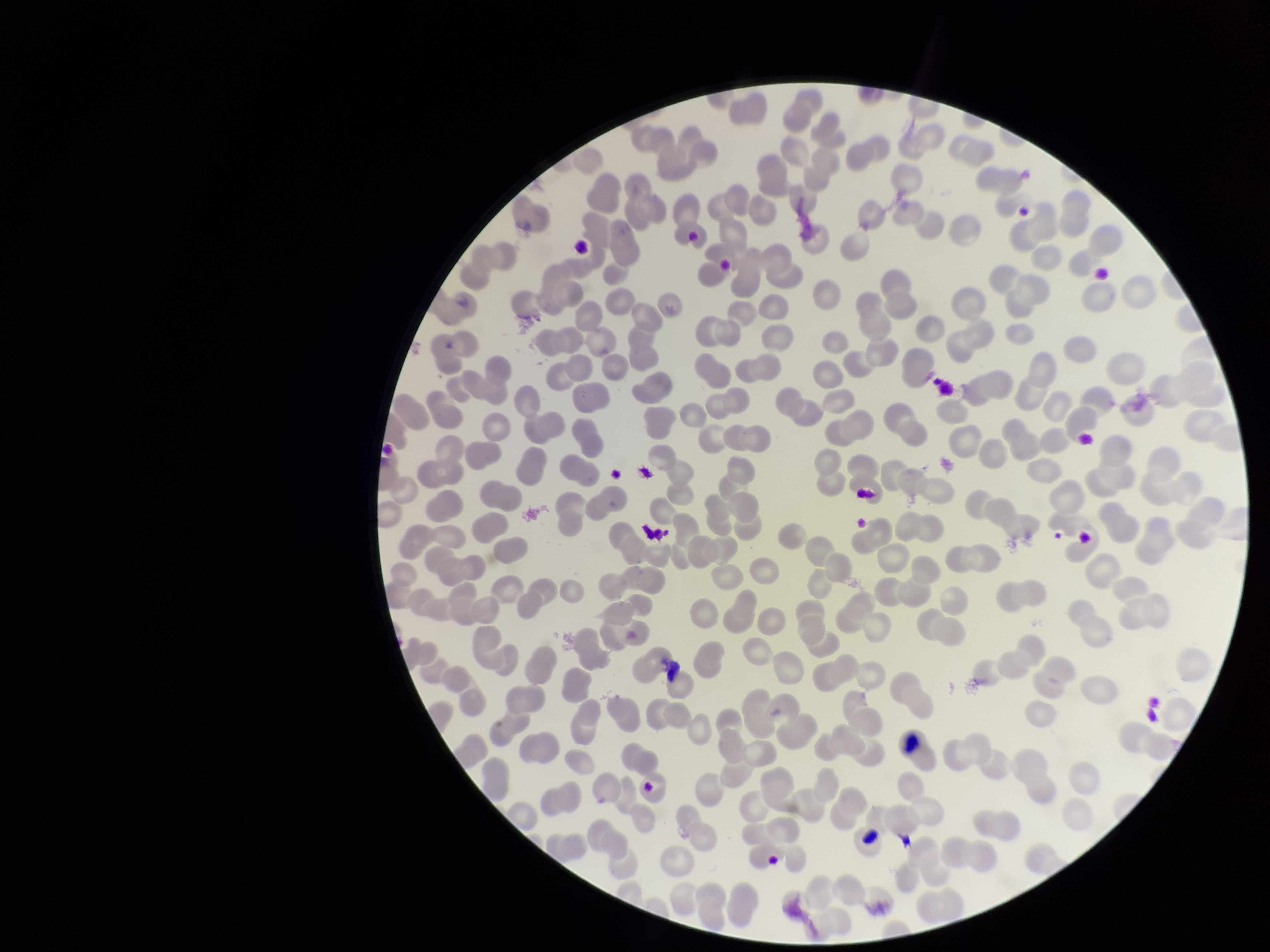

Summary:
  - Image size: 1270×952 pixels
  - Patient malaria status: negative
  - Preparation: thin blood smear
  - Parasitized red blood cell count: 0
  - Red blood cell count: 267
  - Parasitized red blood cells: none seen
  - Field of view: single
  - Capture: smartphone photograph through the microscope eyepiece
  - Stain: Giemsa